Mark where platelets are.
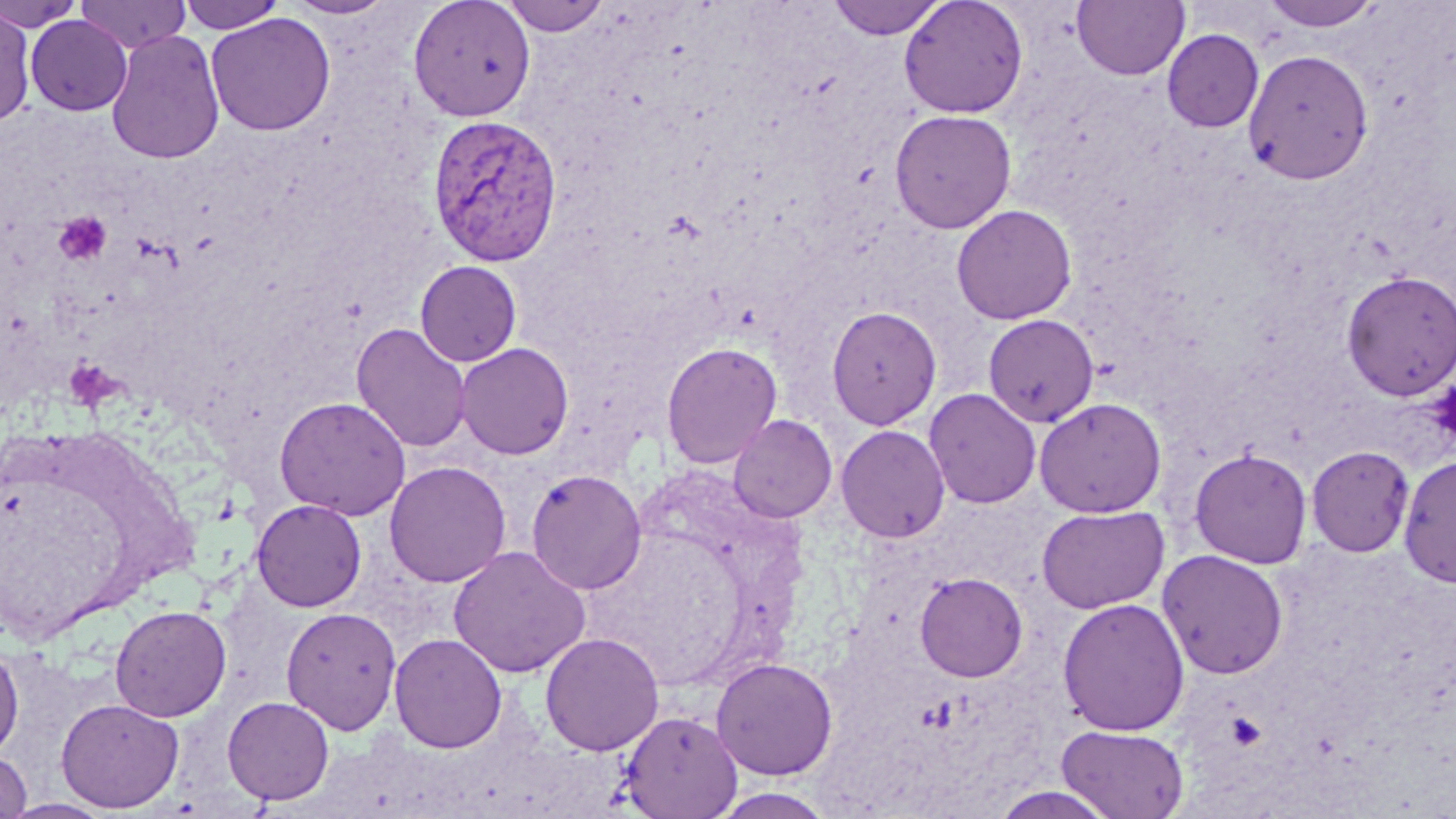
Approximate bounding boxes as named x1/y1/x2/y2 corners in pixels.
Platelets: (x1=55, y1=210, x2=112, y2=265), (x1=65, y1=358, x2=119, y2=409), (x1=1425, y1=379, x2=1456, y2=446).

Uninfected red blood cell locations: (x1=0, y1=0, x2=83, y2=31), (x1=76, y1=0, x2=191, y2=54), (x1=178, y1=0, x2=286, y2=33), (x1=284, y1=0, x2=397, y2=20), (x1=407, y1=0, x2=536, y2=122), (x1=500, y1=0, x2=611, y2=36), (x1=826, y1=0, x2=950, y2=40), (x1=898, y1=0, x2=1029, y2=118), (x1=1071, y1=0, x2=1190, y2=81), (x1=1262, y1=1, x2=1383, y2=32), (x1=0, y1=7, x2=36, y2=125), (x1=206, y1=13, x2=336, y2=136), (x1=25, y1=15, x2=132, y2=116), (x1=106, y1=29, x2=225, y2=165), (x1=1162, y1=29, x2=1264, y2=132), (x1=1243, y1=48, x2=1374, y2=184), (x1=889, y1=109, x2=1016, y2=234), (x1=952, y1=204, x2=1077, y2=325), (x1=415, y1=260, x2=522, y2=366), (x1=1341, y1=270, x2=1456, y2=400), (x1=412, y1=290, x2=529, y2=425), (x1=826, y1=305, x2=941, y2=430), (x1=983, y1=314, x2=1099, y2=427), (x1=352, y1=323, x2=471, y2=452), (x1=661, y1=341, x2=782, y2=468), (x1=455, y1=342, x2=574, y2=459), (x1=924, y1=388, x2=1041, y2=509), (x1=274, y1=396, x2=411, y2=520), (x1=1034, y1=397, x2=1166, y2=517), (x1=728, y1=414, x2=837, y2=523), (x1=836, y1=424, x2=950, y2=543), (x1=1306, y1=445, x2=1414, y2=557), (x1=1188, y1=447, x2=1313, y2=568), (x1=1398, y1=454, x2=1456, y2=587), (x1=385, y1=461, x2=511, y2=587), (x1=526, y1=469, x2=647, y2=595), (x1=251, y1=499, x2=367, y2=612), (x1=1036, y1=504, x2=1169, y2=614), (x1=448, y1=545, x2=591, y2=679), (x1=1156, y1=549, x2=1289, y2=679), (x1=915, y1=572, x2=1028, y2=682), (x1=1057, y1=597, x2=1190, y2=737), (x1=110, y1=604, x2=231, y2=722), (x1=281, y1=606, x2=401, y2=734), (x1=540, y1=632, x2=665, y2=756), (x1=389, y1=633, x2=507, y2=754), (x1=0, y1=641, x2=24, y2=761), (x1=711, y1=657, x2=838, y2=779), (x1=222, y1=695, x2=334, y2=805), (x1=56, y1=697, x2=184, y2=813), (x1=618, y1=711, x2=742, y2=819), (x1=1056, y1=724, x2=1189, y2=819), (x1=0, y1=751, x2=32, y2=818), (x1=987, y1=785, x2=1122, y2=819), (x1=709, y1=787, x2=837, y2=818), (x1=3, y1=798, x2=113, y2=818). Plasmodium vivax-infected red blood cell locations: (x1=427, y1=114, x2=563, y2=266). Slide-level diagnosis: Plasmodium vivax. Thin blood film. 1000x magnification. Single field of view. Light microscopy. Image is 1456×819 pixels. May-Grünwald-Giemsa stain.